Comment on the morphology of the erythrocytes.
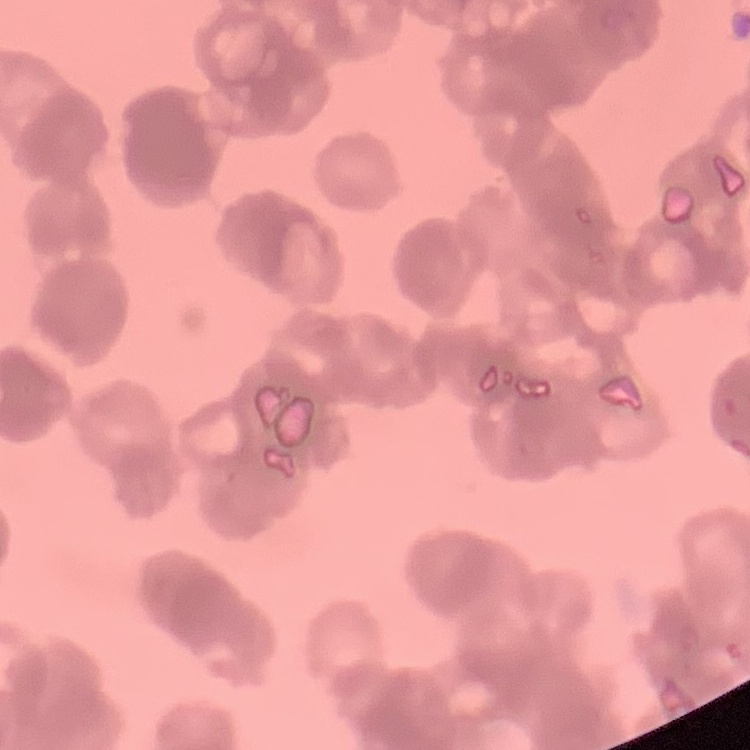
They show rouleaux formation.

{
  "preparation": "thin blood film",
  "image_type": "one tile cut from a larger photomicrograph",
  "stain": "Field's or Giemsa"
}